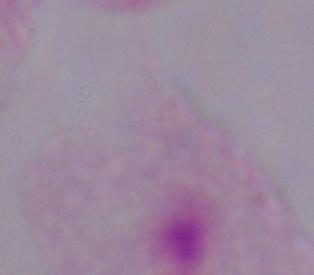
Photomicrograph. A trichomonad is shown. 1000x magnification.